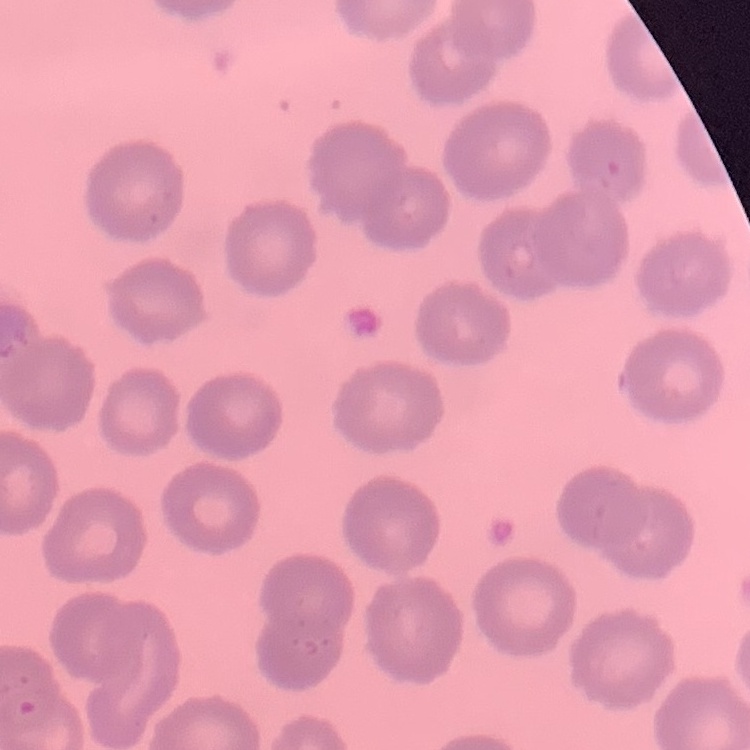

erythrocyte_morphology: no rouleaux formation
preparation: thin blood smear
image_type: one tile cut from a larger photomicrograph
stain: Field's or Giemsa